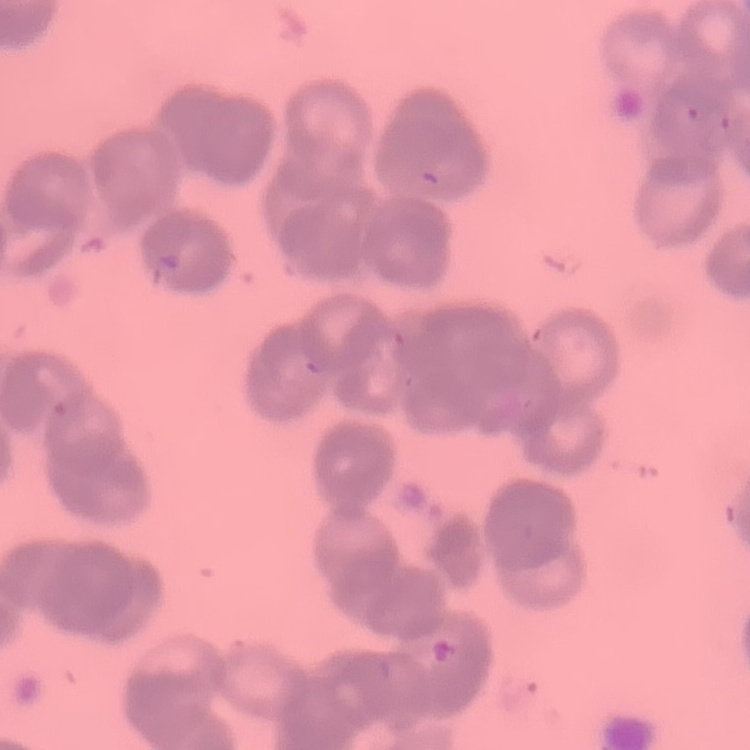

Summary:
  - Red blood cell morphology: rouleaux formation
  - Preparation: thin blood film
  - Stain: Field's or Giemsa
  - Image type: square crop of a larger photomicrograph